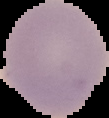

Summary:
  - Malaria status: uninfected
  - Image size: 109×118 pixels
  - Image type: segmented cell region with the area outside set to black
  - Preparation: thin blood smear